Point out each leukocyte.
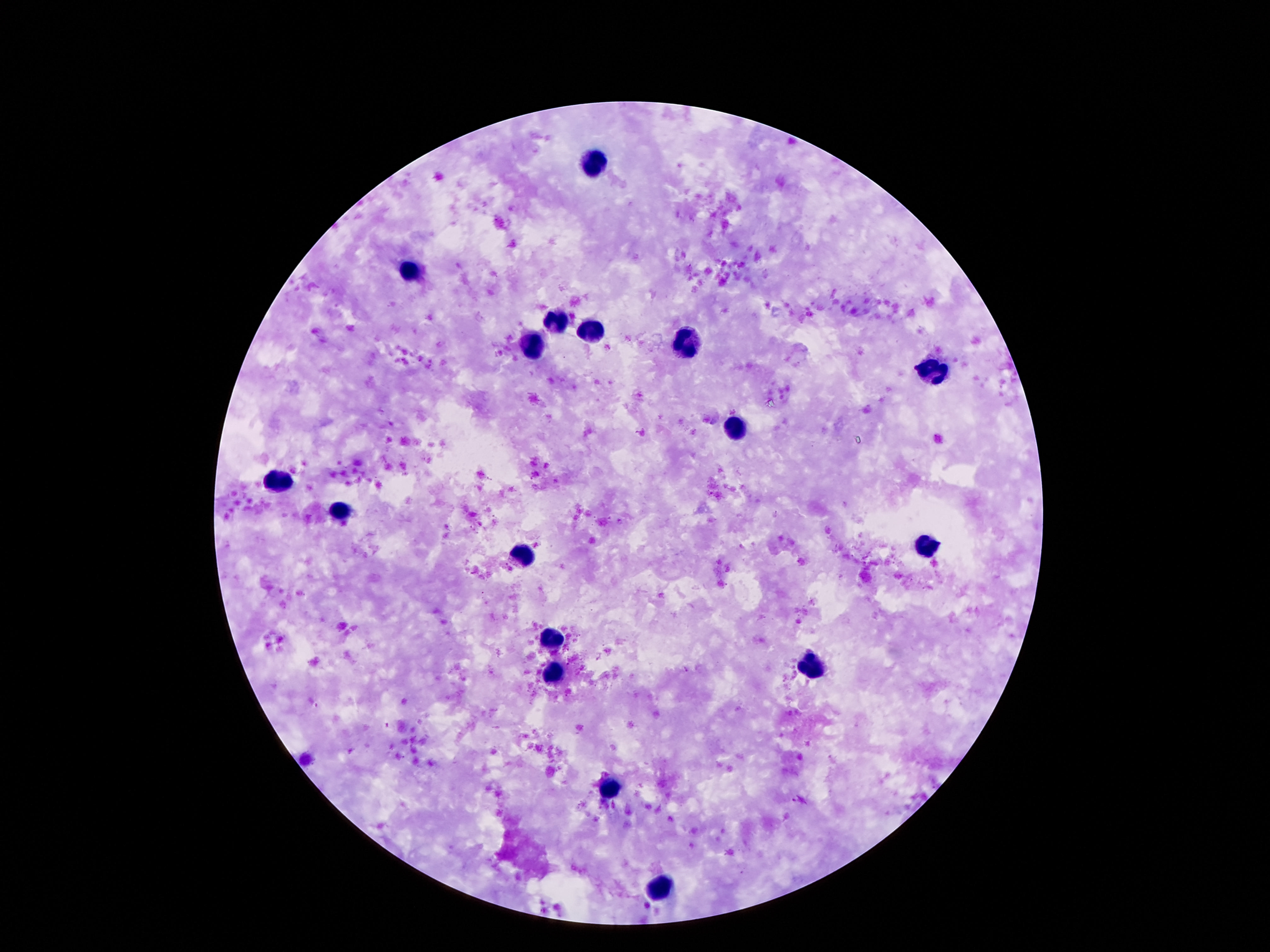

Approximate centers as {x, y} in pixels.
Leukocytes: {597, 162}, {412, 270}, {557, 320}, {592, 334}, {686, 344}, {531, 349}, {924, 372}, {740, 426}, {278, 483}, {340, 511}, {926, 547}, {523, 555}, {548, 637}, {807, 665}, {555, 675}, {610, 790}, {659, 889}.

Smartphone photograph taken through the microscope eyepiece. Image is 1270×952 pixels. Single field of view. Giemsa-stained preparation. Thick blood smear. 100x magnification. Patient malaria status: not infected.